Outline each blood parasite and name the species.
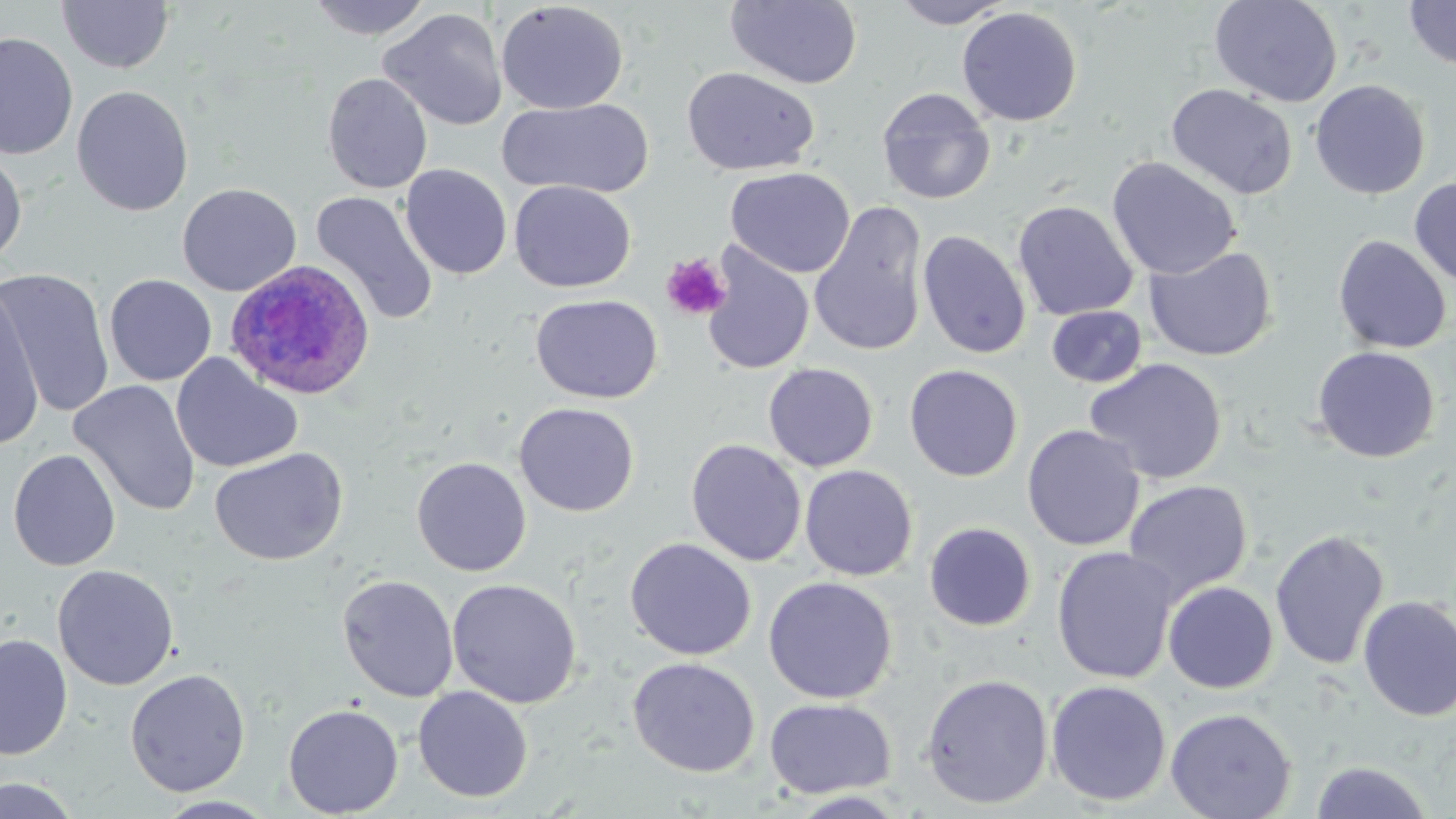
Approximate bounding boxes as named x1/y1/x2/y2 corners in pixels.
Plasmodium ovale-infected red blood cells: (x1=224, y1=259, x2=376, y2=401).
No Plasmodium falciparum, Plasmodium malariae, Plasmodium vivax, Babesia divergens, or Trypanosoma brucei observed.

slide-level diagnosis = Plasmodium ovale
preparation = thin blood smear
field of view = single
uninfected red blood cell locations = approximate bounding boxes as named x1/y1/x2/y2 corners in pixels: (x1=57, y1=0, x2=174, y2=75), (x1=306, y1=0, x2=432, y2=40), (x1=726, y1=0, x2=864, y2=89), (x1=890, y1=0, x2=1013, y2=28), (x1=1209, y1=0, x2=1343, y2=107), (x1=496, y1=1, x2=629, y2=114), (x1=1403, y1=1, x2=1456, y2=71), (x1=957, y1=6, x2=1082, y2=127), (x1=378, y1=7, x2=508, y2=132), (x1=0, y1=31, x2=79, y2=161), (x1=681, y1=66, x2=819, y2=176), (x1=321, y1=72, x2=434, y2=194), (x1=1309, y1=79, x2=1430, y2=199), (x1=1166, y1=83, x2=1298, y2=200), (x1=71, y1=85, x2=194, y2=217), (x1=876, y1=87, x2=996, y2=205), (x1=498, y1=98, x2=655, y2=199), (x1=0, y1=145, x2=28, y2=268), (x1=1107, y1=156, x2=1242, y2=280), (x1=400, y1=163, x2=512, y2=280), (x1=725, y1=167, x2=855, y2=278), (x1=1409, y1=176, x2=1456, y2=289), (x1=509, y1=180, x2=636, y2=292), (x1=177, y1=183, x2=302, y2=297), (x1=310, y1=190, x2=438, y2=325), (x1=1012, y1=200, x2=1139, y2=321), (x1=808, y1=201, x2=929, y2=357), (x1=917, y1=230, x2=1031, y2=359), (x1=1332, y1=234, x2=1452, y2=354), (x1=700, y1=243, x2=815, y2=376), (x1=1144, y1=245, x2=1278, y2=362), (x1=1, y1=268, x2=114, y2=417), (x1=104, y1=274, x2=217, y2=386), (x1=0, y1=280, x2=45, y2=449), (x1=531, y1=294, x2=663, y2=404), (x1=1046, y1=305, x2=1147, y2=388), (x1=1312, y1=346, x2=1440, y2=463), (x1=170, y1=352, x2=303, y2=474), (x1=1084, y1=358, x2=1227, y2=485), (x1=763, y1=363, x2=878, y2=472), (x1=904, y1=364, x2=1023, y2=482), (x1=68, y1=379, x2=201, y2=517), (x1=514, y1=402, x2=640, y2=517), (x1=1022, y1=424, x2=1145, y2=551), (x1=685, y1=438, x2=806, y2=567), (x1=208, y1=447, x2=349, y2=565), (x1=7, y1=449, x2=121, y2=571), (x1=411, y1=457, x2=531, y2=577), (x1=799, y1=464, x2=918, y2=581), (x1=1123, y1=479, x2=1253, y2=602), (x1=924, y1=522, x2=1036, y2=631), (x1=1269, y1=528, x2=1390, y2=670), (x1=624, y1=537, x2=757, y2=661), (x1=1051, y1=546, x2=1179, y2=684), (x1=52, y1=564, x2=179, y2=691), (x1=337, y1=574, x2=459, y2=702), (x1=763, y1=576, x2=898, y2=704), (x1=446, y1=579, x2=582, y2=708), (x1=1163, y1=581, x2=1279, y2=694), (x1=1357, y1=595, x2=1456, y2=722), (x1=0, y1=633, x2=73, y2=760), (x1=627, y1=657, x2=760, y2=777), (x1=125, y1=668, x2=251, y2=797), (x1=919, y1=673, x2=1054, y2=809), (x1=1045, y1=679, x2=1171, y2=807), (x1=413, y1=685, x2=533, y2=802), (x1=764, y1=697, x2=896, y2=799), (x1=283, y1=703, x2=404, y2=817), (x1=1165, y1=707, x2=1297, y2=819), (x1=1310, y1=760, x2=1433, y2=818), (x1=0, y1=774, x2=83, y2=818), (x1=788, y1=791, x2=909, y2=818), (x1=153, y1=795, x2=278, y2=819)
image size = 1456×819 pixels
platelet locations = approximate bounding boxes as named x1/y1/x2/y2 corners in pixels: (x1=660, y1=253, x2=731, y2=321)
modality = optical microscopy
magnification = 1000x
stain = May-Grünwald-Giemsa